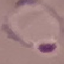

Result: malaria parasites identified. Giemsa stain. Cell patch, automatically extracted from a larger field of view and resized to 64 × 64 pixels. Photographed with a smartphone camera at the microscope eyepiece. Thin blood film.